Name the cell type shown.
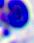

A leukocyte.

modality = micrograph
magnification = 400x